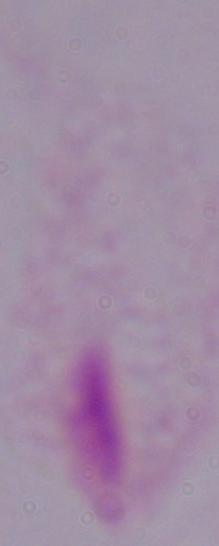
modality = photomicrograph
magnification = 1000x
identification = trichomonad